Name the parasite shown.
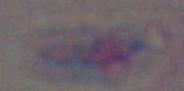

This is Toxoplasma gondii.

Micrograph. Captured at 1000x magnification.